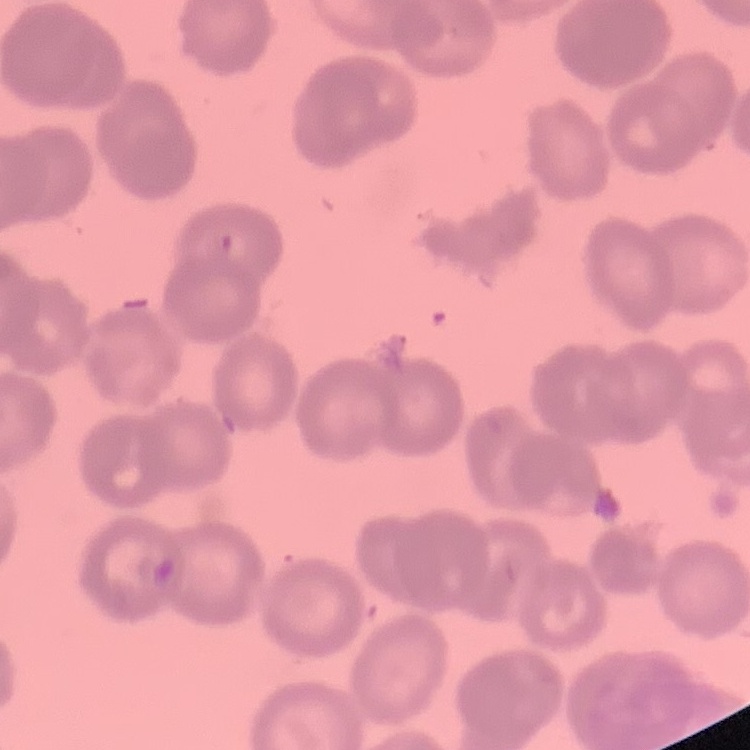
erythrocyte morphology = rouleaux formation
stain = Field's or Giemsa
preparation = thin peripheral smear
image type = square crop of a larger photomicrograph